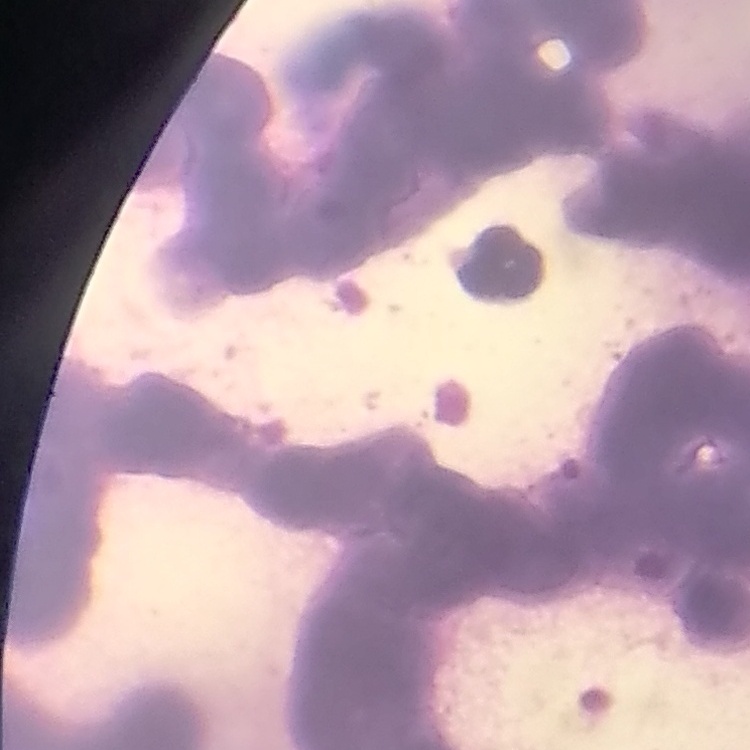

erythrocyte morphology = rouleaux formation
preparation = thin blood smear
image type = one tile cut from a larger photomicrograph
stain = Field's or Giemsa